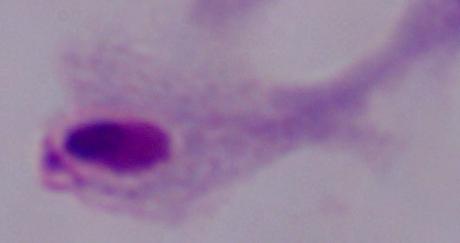

{
  "modality": "micrograph",
  "identification": "trichomonad",
  "magnification": "1000x"
}